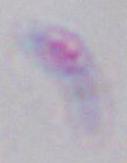
modality: photomicrograph
identification: Toxoplasma gondii
magnification: 1000x